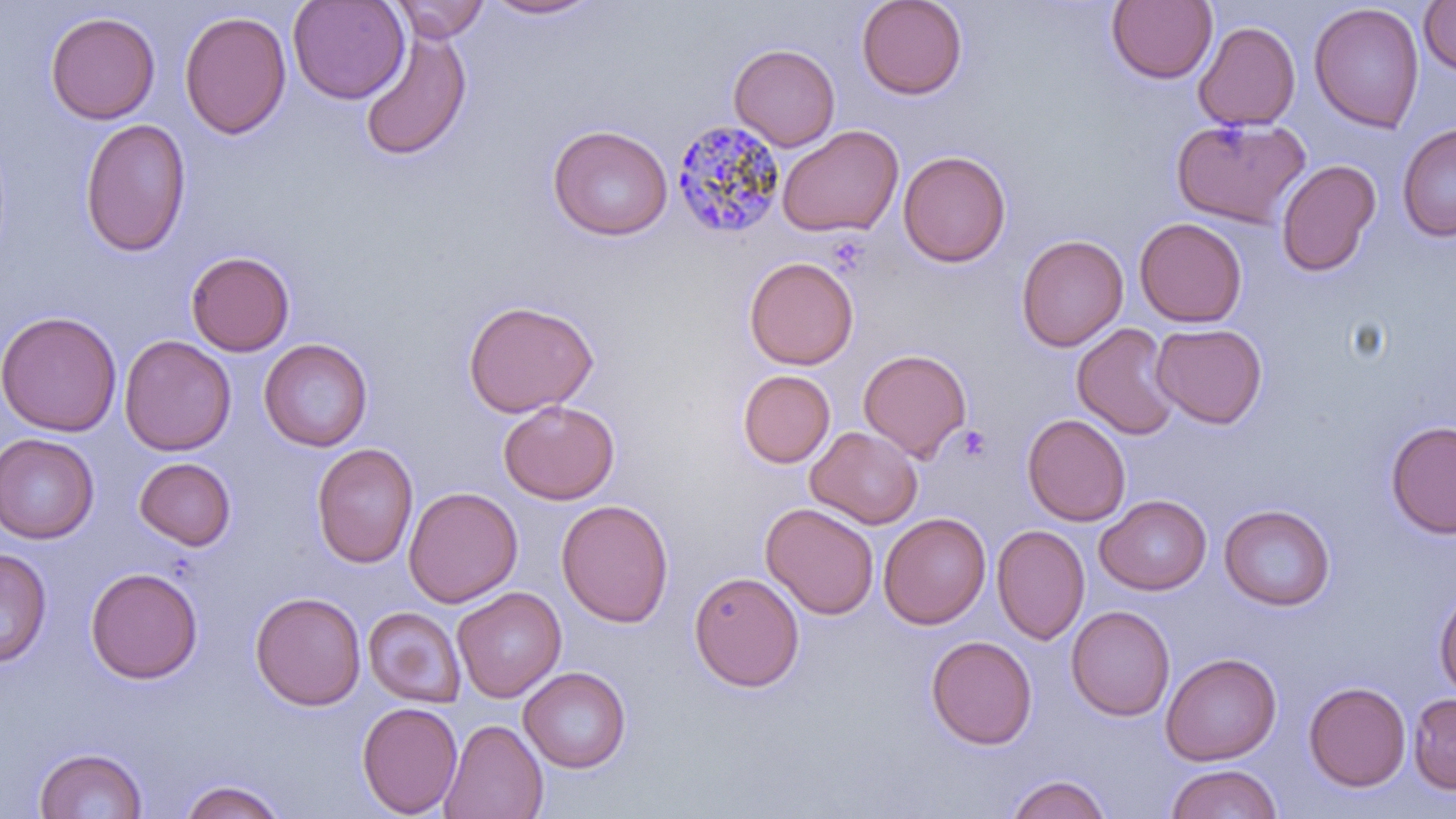 Approximate bounding boxes as named x1/y1/x2/y2 corners in pixels. Uninfected red blood cell locations: (x1=287, y1=0, x2=410, y2=104), (x1=390, y1=0, x2=490, y2=43), (x1=483, y1=0, x2=602, y2=20), (x1=856, y1=0, x2=967, y2=100), (x1=1107, y1=0, x2=1217, y2=84), (x1=1418, y1=1, x2=1456, y2=76), (x1=1309, y1=3, x2=1425, y2=133), (x1=179, y1=9, x2=291, y2=140), (x1=45, y1=11, x2=160, y2=124), (x1=1194, y1=21, x2=1300, y2=130), (x1=358, y1=26, x2=472, y2=162), (x1=728, y1=43, x2=840, y2=151), (x1=1172, y1=116, x2=1310, y2=228), (x1=79, y1=118, x2=192, y2=257), (x1=1397, y1=123, x2=1456, y2=241), (x1=547, y1=124, x2=672, y2=241), (x1=776, y1=125, x2=903, y2=238), (x1=898, y1=150, x2=1012, y2=267), (x1=1276, y1=159, x2=1381, y2=277), (x1=1134, y1=218, x2=1247, y2=327), (x1=1015, y1=234, x2=1128, y2=352), (x1=186, y1=250, x2=294, y2=356), (x1=743, y1=256, x2=859, y2=371), (x1=462, y1=299, x2=599, y2=417), (x1=0, y1=311, x2=121, y2=436), (x1=1072, y1=322, x2=1180, y2=440), (x1=1151, y1=323, x2=1267, y2=428), (x1=119, y1=335, x2=236, y2=456), (x1=259, y1=338, x2=373, y2=452), (x1=858, y1=348, x2=972, y2=461), (x1=738, y1=370, x2=835, y2=468), (x1=498, y1=399, x2=620, y2=504), (x1=1022, y1=413, x2=1131, y2=526), (x1=1385, y1=419, x2=1456, y2=539), (x1=806, y1=426, x2=923, y2=529), (x1=0, y1=433, x2=100, y2=544), (x1=311, y1=443, x2=418, y2=569), (x1=133, y1=457, x2=237, y2=551), (x1=403, y1=486, x2=522, y2=607), (x1=1095, y1=495, x2=1211, y2=595), (x1=556, y1=498, x2=674, y2=627), (x1=760, y1=502, x2=879, y2=620), (x1=1219, y1=504, x2=1336, y2=610), (x1=878, y1=512, x2=991, y2=629), (x1=992, y1=524, x2=1090, y2=645), (x1=0, y1=548, x2=52, y2=667), (x1=85, y1=566, x2=203, y2=684), (x1=689, y1=571, x2=804, y2=692), (x1=1434, y1=585, x2=1456, y2=699), (x1=452, y1=586, x2=566, y2=702), (x1=250, y1=591, x2=365, y2=711), (x1=1066, y1=605, x2=1175, y2=721), (x1=363, y1=606, x2=466, y2=707), (x1=926, y1=635, x2=1037, y2=750), (x1=1160, y1=652, x2=1282, y2=766), (x1=519, y1=666, x2=631, y2=772), (x1=1304, y1=681, x2=1411, y2=792), (x1=1408, y1=692, x2=1456, y2=795), (x1=356, y1=701, x2=463, y2=817), (x1=439, y1=718, x2=548, y2=819), (x1=34, y1=747, x2=147, y2=819), (x1=1165, y1=764, x2=1283, y2=819), (x1=1006, y1=774, x2=1112, y2=819), (x1=178, y1=778, x2=287, y2=819). Plasmodium malariae-infected red blood cell locations: (x1=671, y1=117, x2=786, y2=240). Platelet locations: (x1=957, y1=425, x2=991, y2=461). Slide-level diagnosis: Plasmodium malariae. Image is 1456×819 pixels. One field of a larger specimen. May-Grünwald-Giemsa stain. Thin blood smear. Light microscopy. Captured at 1000x magnification.